Locate every parasitized red blood cell.
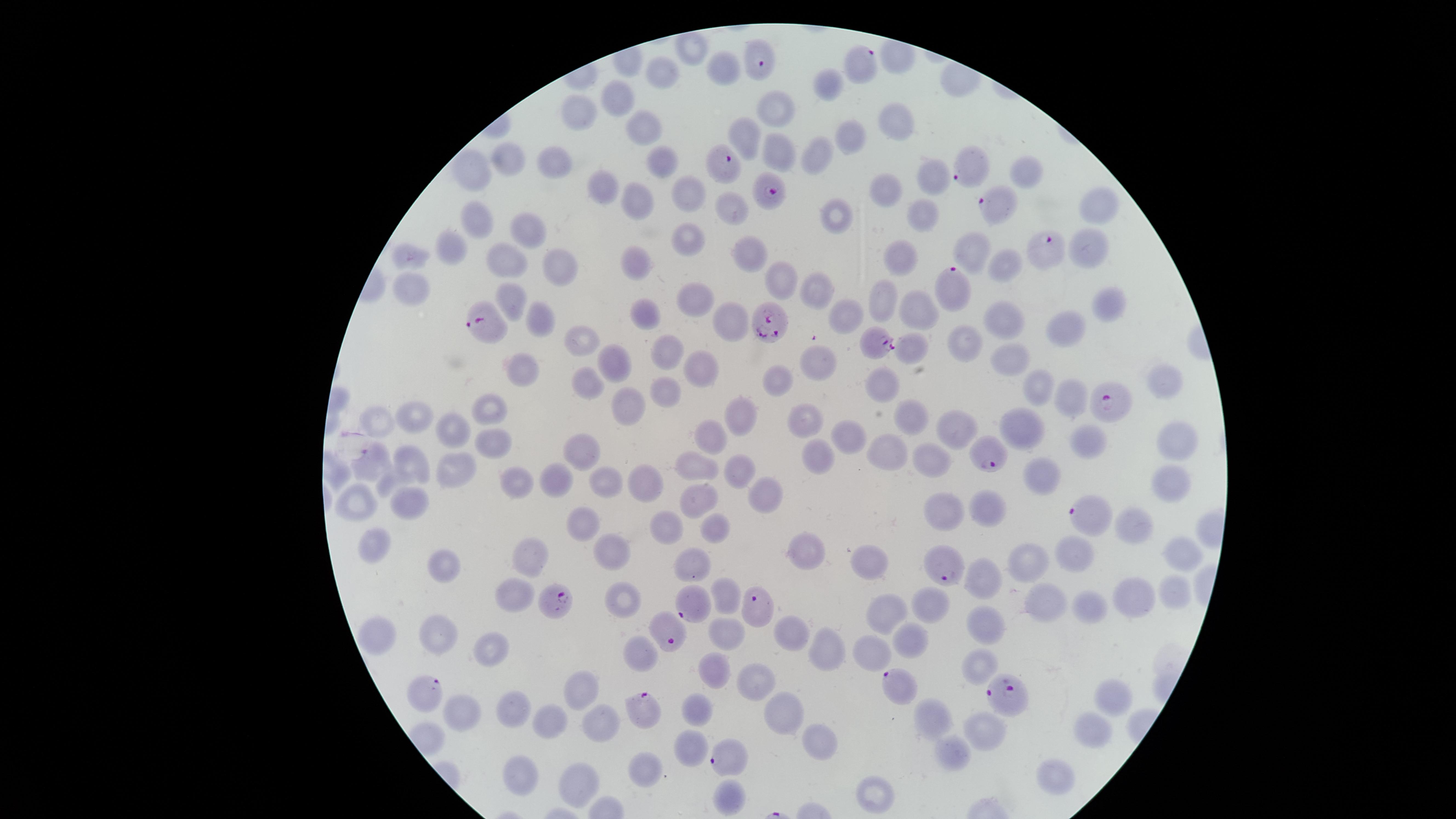

Approximate marker points as [x, y] in pixels.
Parasitized red blood cells: [758, 60], [862, 62], [720, 163], [971, 166], [770, 191], [1000, 204], [1045, 248], [952, 288], [491, 321], [769, 323], [875, 342], [1109, 402], [991, 453], [1087, 514], [945, 572], [558, 598], [691, 608], [757, 610], [666, 634], [897, 685], [425, 695], [1007, 696], [643, 711], [724, 757].

uninfected_red_blood_cells: 'approximate marker points as [x, y] in pixels: [693, 48], [727, 68], [663, 71], [825, 83], [622, 96], [782, 107], [588, 110], [893, 127], [641, 128], [750, 134], [856, 140], [779, 151], [818, 153], [511, 160], [555, 162], [669, 165], [1029, 169], [477, 170], [931, 177], [602, 185], [884, 188], [684, 192], [640, 193], [1101, 205], [734, 207], [478, 215], [835, 216], [928, 216], [525, 228], [690, 236], [452, 240], [1086, 242], [971, 248], [750, 251], [414, 257], [901, 260], [510, 262], [638, 263], [565, 265], [997, 265], [782, 276], [414, 288], [814, 290], [514, 293], [700, 294], [879, 294], [1110, 301], [647, 307], [924, 308], [856, 312], [543, 314], [731, 320], [1008, 321], [1063, 328], [579, 337], [968, 340], [918, 346], [669, 350], [818, 356], [1008, 357], [701, 367], [525, 369], [773, 378], [883, 381], [1161, 381], [588, 384], [672, 387], [1040, 390], [1067, 392], [627, 404], [915, 411], [493, 412], [417, 413], [739, 415], [1019, 416], [381, 417], [809, 418], [951, 423], [453, 426], [858, 433], [1181, 437], [712, 438], [1092, 439], [494, 444], [588, 452], [894, 452], [931, 454], [817, 455], [378, 459], [695, 463], [739, 463], [414, 465], [452, 474], [1044, 474], [556, 476], [647, 478], [522, 479], [610, 482], [1172, 483], [767, 494], [356, 501], [698, 501], [982, 503], [407, 504], [943, 509], [1136, 515], [581, 522], [718, 527], [669, 528], [378, 546], [611, 548], [1076, 552], [1179, 552], [805, 554], [523, 559], [1034, 561], [693, 563], [870, 565], [449, 568], [984, 579], [1172, 588], [729, 591], [512, 593], [622, 596], [932, 598], [1134, 599], [1050, 602], [1091, 610], [883, 617], [440, 626], [989, 628], [379, 629], [791, 632], [724, 636], [908, 639], [493, 648], [874, 651], [828, 653], [639, 656], [982, 664], [715, 671], [758, 679], [580, 686], [1112, 699], [700, 708], [468, 709], [780, 709], [515, 710], [939, 718], [555, 721], [595, 722], [1093, 729], [987, 735], [817, 737], [691, 747], [955, 749], [523, 771], [653, 773], [1058, 780], [584, 781], [731, 792], [874, 795]'
stain: Giemsa
preparation: thin blood film
image_size: 1456×819 pixels
species: Plasmodium falciparum
field_of_view: single
visible_region: circular
capture: smartphone photograph through the microscope eyepiece